Locate every malaria parasite.
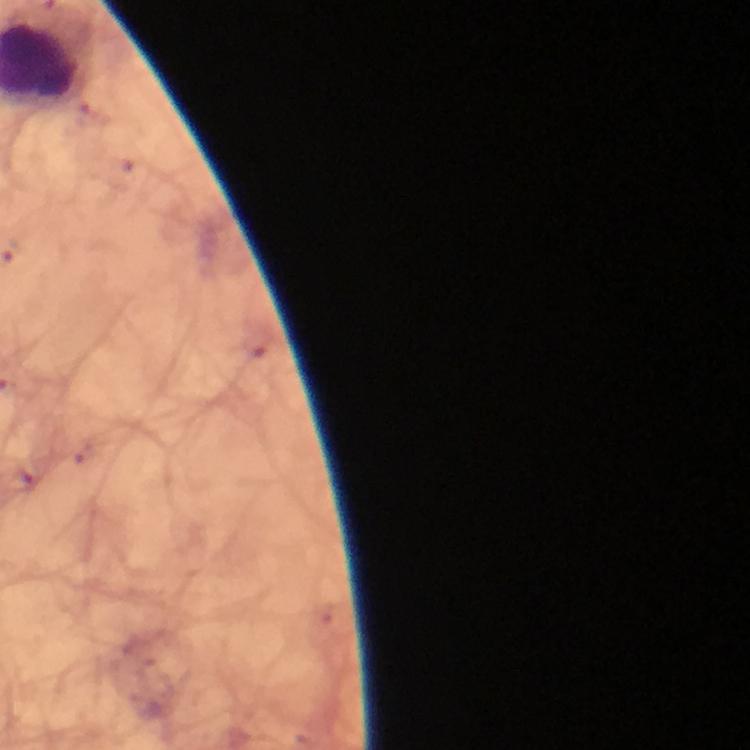

Approximate centers as {x, y} in pixels.
Malaria parasites: {258, 342}.

A crop from one field of view. Immersion oil was used. Image is 750×750 pixels. Giemsa stain. Photographed through the microscope with a smartphone camera. Thick blood smear. At 100x magnification. From a malaria diagnostic workup.